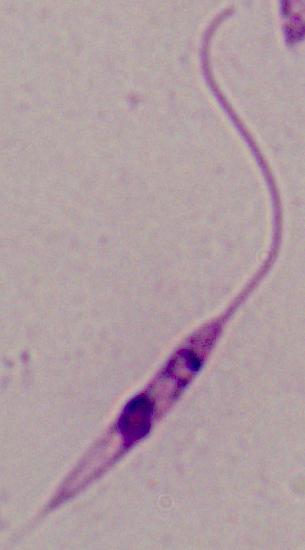
identification = Leishmania
magnification = 1000x
modality = photomicrograph